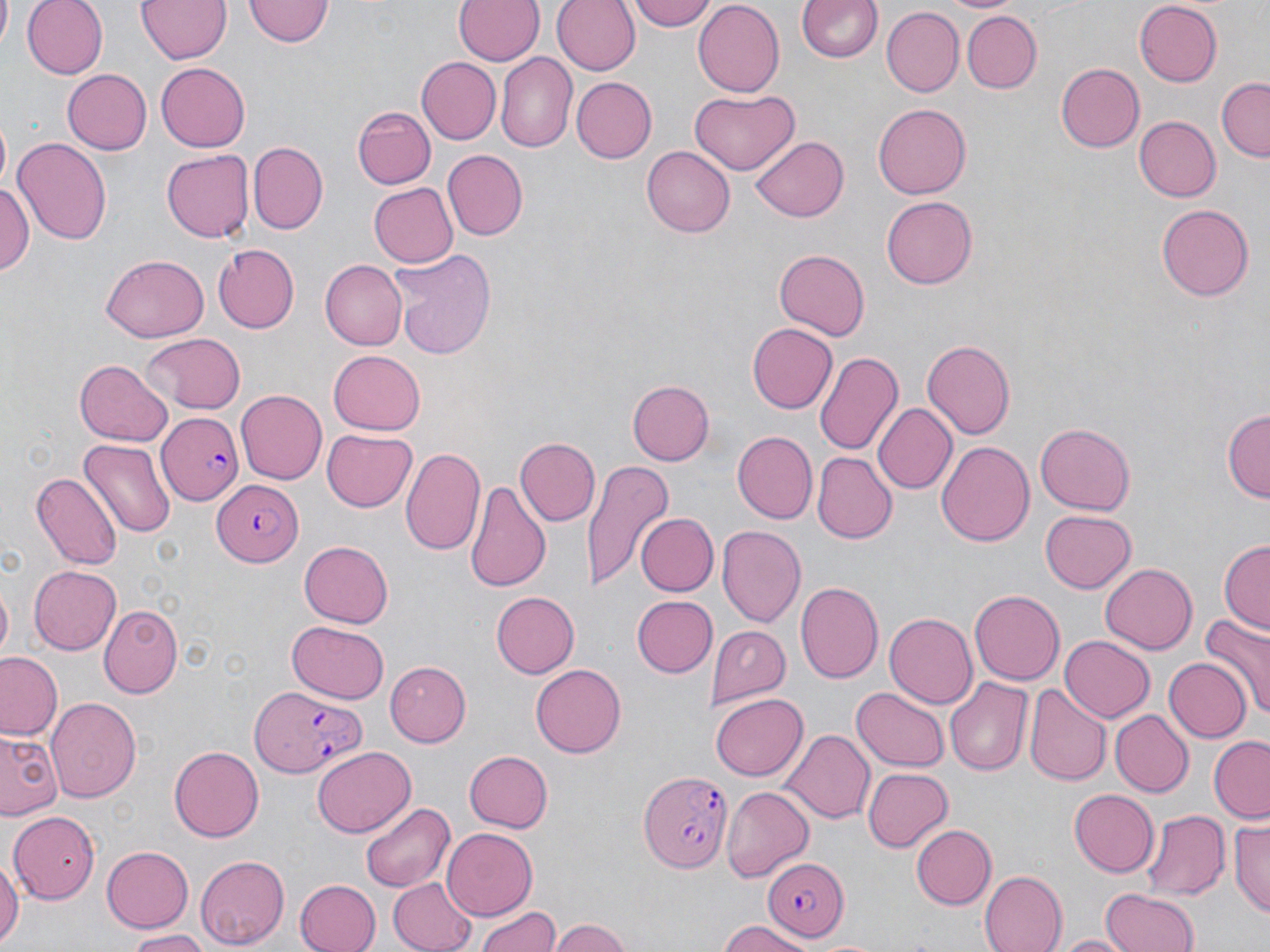
slide-level diagnosis = Plasmodium falciparum
uninfected red blood cell locations = approximate bounding boxes as [x1, y1, x2, y2] in pixels: [22, 0, 106, 78], [136, 0, 231, 63], [454, 0, 543, 67], [551, 0, 640, 75], [628, 0, 715, 29], [245, 1, 331, 48], [691, 1, 782, 96], [798, 1, 883, 65], [1135, 2, 1223, 87], [883, 8, 963, 96], [964, 12, 1042, 93], [495, 53, 577, 153], [416, 57, 499, 143], [154, 63, 249, 151], [1055, 63, 1145, 153], [60, 69, 150, 155], [570, 77, 655, 163], [1215, 78, 1269, 161], [691, 87, 799, 175], [873, 102, 970, 199], [353, 106, 435, 188], [1135, 116, 1220, 201], [751, 136, 849, 221], [11, 137, 111, 241], [248, 142, 328, 233], [642, 147, 734, 237], [443, 150, 527, 241], [161, 151, 253, 242], [1, 180, 34, 279], [369, 181, 459, 268], [882, 195, 977, 289], [1155, 204, 1253, 301], [212, 245, 300, 332], [389, 248, 498, 359], [773, 248, 870, 340], [101, 253, 208, 341], [319, 259, 405, 350], [747, 323, 837, 413], [141, 333, 246, 413], [923, 338, 1016, 438], [814, 349, 903, 456], [327, 351, 425, 435], [75, 358, 171, 444], [628, 380, 714, 466], [235, 390, 325, 485], [873, 404, 955, 493], [1223, 408, 1269, 504], [1035, 422, 1135, 514], [323, 429, 417, 512], [731, 431, 817, 523], [517, 435, 598, 526], [79, 438, 177, 537], [937, 440, 1035, 547], [401, 448, 486, 558], [812, 453, 895, 543], [584, 460, 673, 592], [30, 471, 121, 572], [464, 479, 554, 591], [1039, 510, 1135, 593], [636, 512, 716, 593], [717, 526, 807, 627], [1218, 538, 1270, 634], [297, 542, 393, 628], [1101, 563, 1197, 655], [27, 564, 120, 655], [795, 581, 884, 683], [969, 590, 1065, 685], [490, 591, 577, 679], [630, 595, 715, 678], [100, 604, 181, 697], [1202, 613, 1270, 718], [883, 614, 976, 709], [285, 620, 392, 705], [710, 626, 793, 704], [1059, 636, 1153, 723], [0, 653, 62, 740], [1164, 656, 1251, 743], [384, 660, 470, 744], [530, 663, 626, 758], [946, 677, 1032, 776], [1025, 684, 1110, 786], [852, 687, 949, 772], [711, 694, 807, 781], [46, 697, 142, 803], [1110, 710, 1192, 797], [0, 727, 63, 821], [779, 728, 874, 824], [1208, 736, 1270, 823], [168, 744, 263, 838], [311, 746, 417, 837], [461, 748, 554, 833], [862, 768, 954, 852], [722, 786, 814, 883], [1069, 789, 1159, 877], [357, 801, 455, 893], [9, 811, 98, 903], [1140, 811, 1228, 901], [1230, 819, 1270, 919], [912, 825, 997, 908], [442, 829, 537, 916], [101, 846, 195, 931], [0, 851, 20, 951], [195, 855, 291, 949], [977, 871, 1067, 952], [387, 875, 480, 952], [295, 877, 382, 952], [1100, 886, 1199, 952], [478, 905, 563, 952], [549, 918, 634, 952], [714, 920, 811, 952], [122, 930, 215, 951], [1052, 933, 1135, 952]
preparation = thin blood film
magnification = 1000x
Plasmodium falciparum-infected red blood cell locations = approximate bounding boxes as [x1, y1, x2, y2] in pixels: [153, 405, 245, 508], [212, 481, 307, 565], [248, 684, 371, 776], [640, 771, 735, 873], [759, 858, 848, 940]
field of view = single
stain = May-Grünwald-Giemsa
modality = light microscopy
image size = 1270×952 pixels